Assess this cell for malaria.
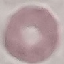

Uninfected.

Thin blood smear. Photographed with a smartphone camera at the microscope eyepiece. Automatically extracted cell patch, resized to 64 × 64 pixels. Giemsa-stained preparation.